Comment on the morphology of the red blood cells.
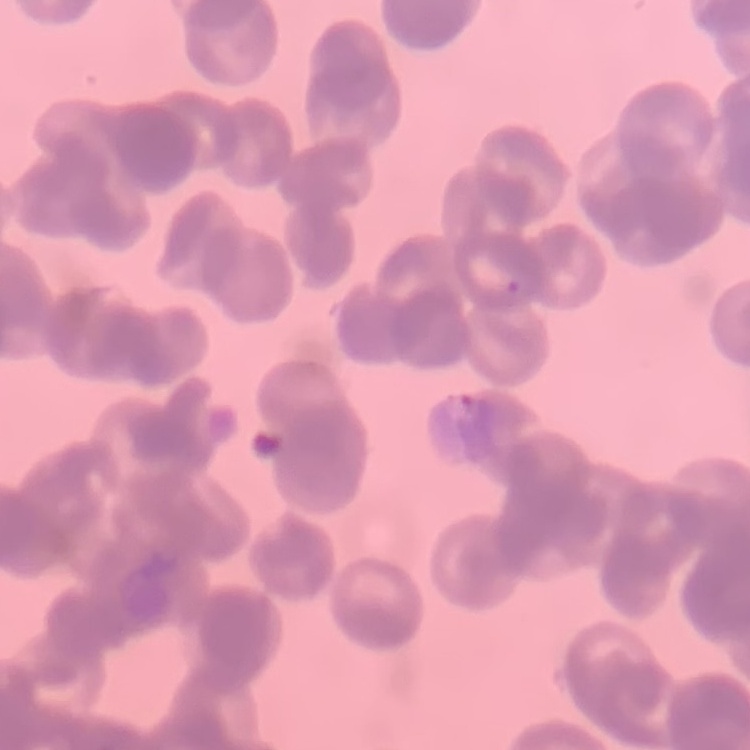
They show rouleaux formation.

Thin peripheral smear. Stained with either Field's or Giemsa. Square crop of a larger photomicrograph.